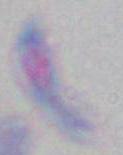
magnification = 1000x
modality = photomicrograph
identification = Toxoplasma gondii